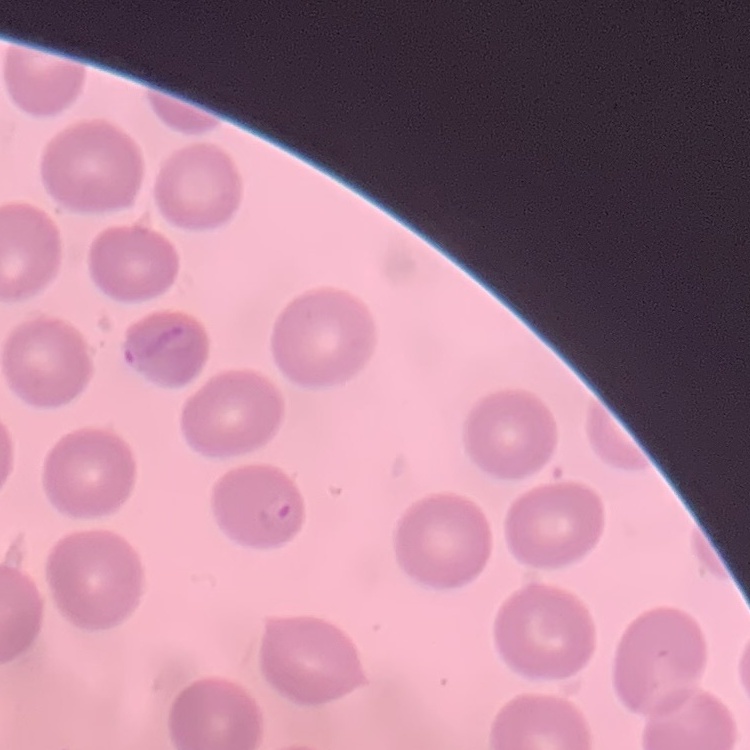

Summary:
  - Red blood cell morphology: no rouleaux formation
  - Image type: square crop of a larger photomicrograph
  - Preparation: thin blood smear
  - Stain: Field's or Giemsa